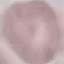

result = no malaria parasites detected
capture = smartphone camera at the microscope eyepiece
preparation = thin blood film
image type = automatically extracted cell patch, resized to 64 × 64 pixels
stain = Giemsa